Comment on the morphology of the red blood cells.
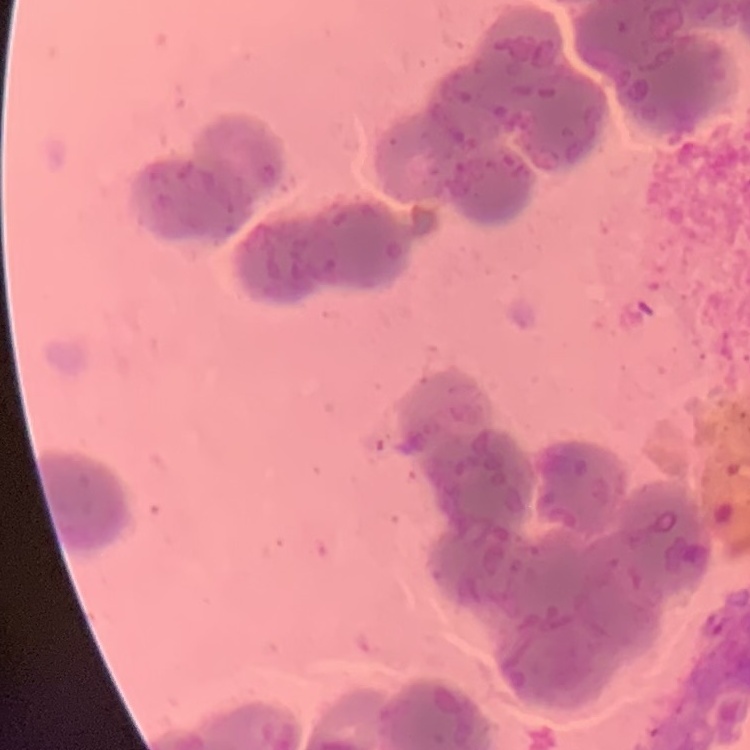
They show rouleaux formation.

Summary:
  - Image type: one tile cut from a larger photomicrograph
  - Stain: Field's or Giemsa
  - Preparation: thin blood smear